Report the malaria status of this cell.
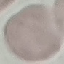

Uninfected.

Giemsa-stained preparation. Thin blood film. Acquired by smartphone through the microscope eyepiece. Automatically extracted cell patch, resized to 64 × 64 pixels.